Assess the morphology of the erythrocytes.
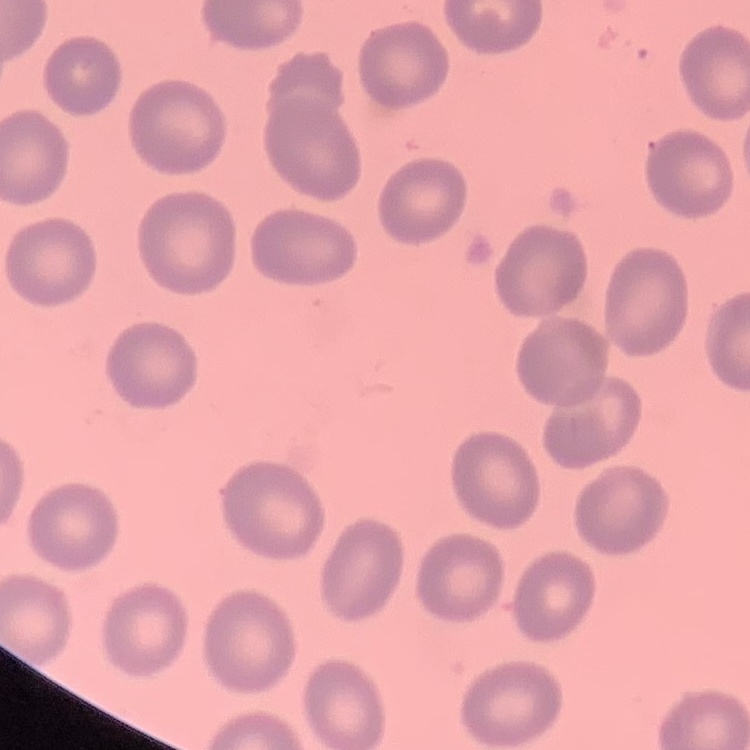
They show no rouleaux formation.

image_type: square crop of a larger photomicrograph
preparation: thin blood smear
stain: Field's or Giemsa